Locate every Plasmodium falciparum-infected red blood cell.
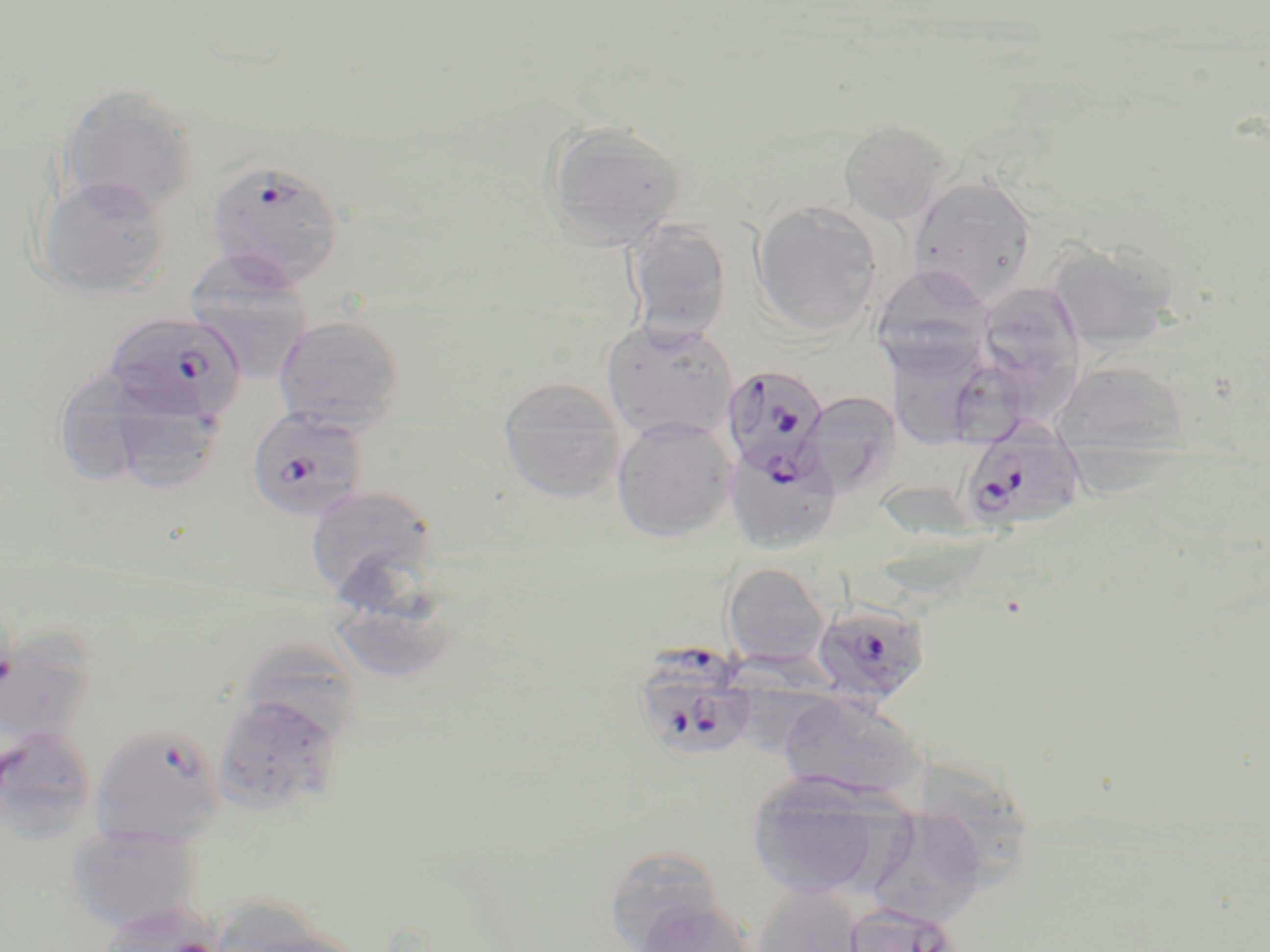

Approximate bounding boxes as [x1, y1, x2, y2] in pixels.
Plasmodium falciparum-infected red blood cells: [206, 159, 346, 290], [103, 311, 246, 424], [720, 364, 831, 483], [246, 407, 368, 522], [966, 420, 1087, 537], [809, 600, 930, 707], [631, 648, 759, 766], [89, 724, 226, 846].

Uninfected red blood cell locations: [60, 84, 199, 217], [542, 120, 687, 249], [838, 121, 951, 225], [907, 174, 1039, 306], [36, 175, 171, 299], [749, 201, 883, 336], [623, 219, 732, 343], [1046, 237, 1180, 353], [184, 251, 314, 382], [871, 264, 992, 373], [980, 283, 1089, 425], [274, 314, 405, 435], [602, 319, 737, 442], [884, 340, 989, 450], [1057, 369, 1188, 496], [51, 370, 161, 491], [497, 377, 626, 503], [799, 391, 901, 499], [105, 393, 227, 494], [611, 417, 736, 543], [726, 447, 843, 553], [305, 485, 439, 603], [721, 563, 831, 667], [0, 624, 99, 737], [212, 690, 346, 816], [777, 693, 927, 803], [0, 728, 102, 843], [923, 760, 1030, 898], [746, 774, 888, 898], [875, 800, 988, 928], [65, 823, 201, 932], [602, 844, 729, 951], [749, 881, 864, 952], [633, 896, 760, 951], [841, 901, 962, 952]. Slide-level diagnosis: Plasmodium falciparum. Image is 1270×952 pixels. Captured at 1000x magnification. Thin blood film. May-Grünwald-Giemsa stain. One field of a larger specimen. Optical microscopy.